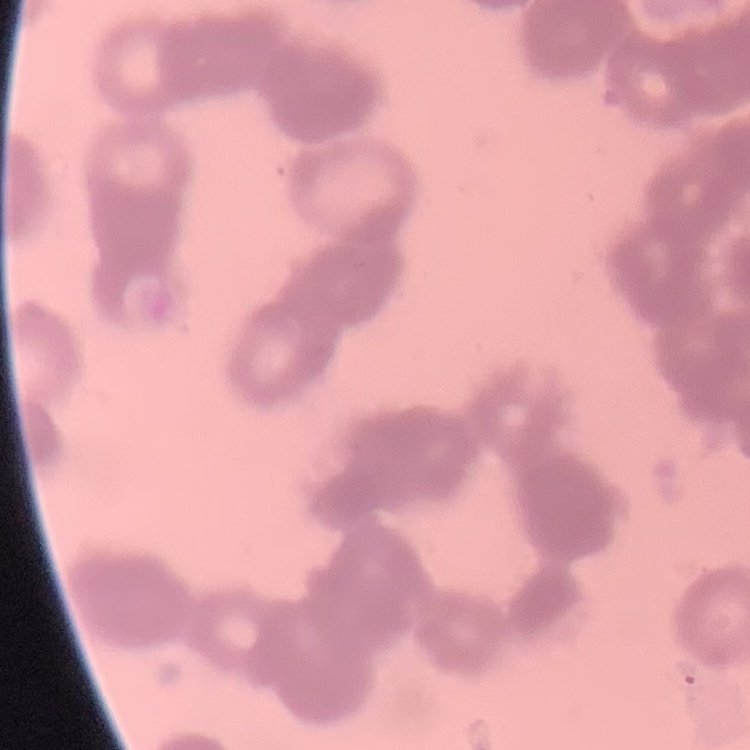
The erythrocytes show rouleaux formation. Stained with either Field's or Giemsa. One tile cut from a larger photomicrograph. Thin peripheral smear.